Assess this cell for malaria.
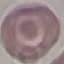
It is uninfected.

capture = smartphone through the microscope eyepiece
image type = cell patch, automatically extracted from a larger field of view and resized to 64 × 64 pixels
preparation = thin blood smear
stain = Giemsa